Locate platelets.
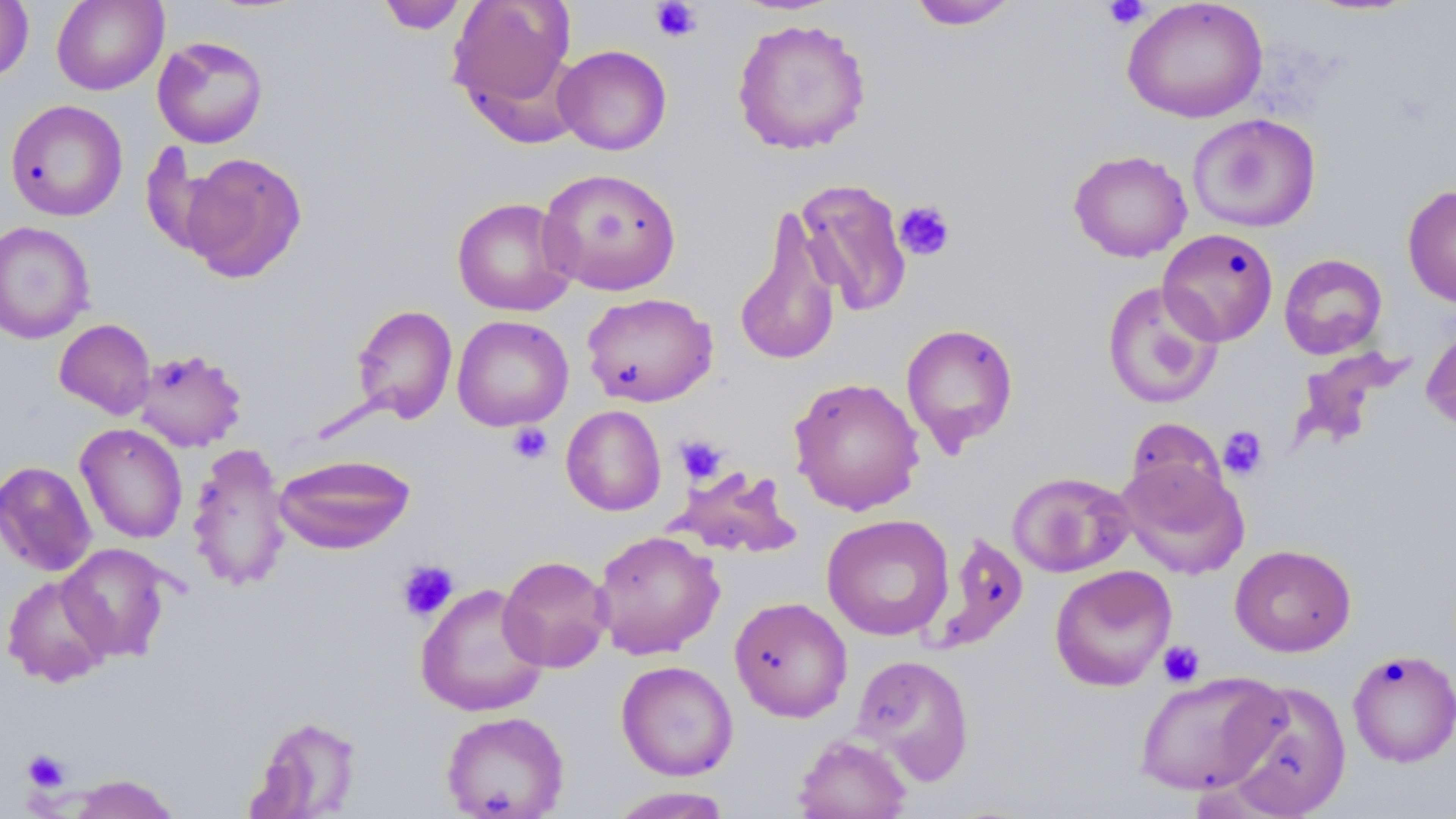

Approximate bounding boxes as (x1, y1, x2, y2) in pixels.
Platelets: (1101, 0, 1151, 31), (649, 1, 703, 43), (893, 200, 956, 260), (507, 422, 552, 465), (1218, 425, 1268, 480), (675, 435, 727, 484), (397, 560, 459, 622), (1157, 640, 1205, 687), (21, 749, 71, 793).

Uninfected red blood cell locations: (0, 0, 34, 82), (52, 0, 168, 95), (447, 0, 579, 122), (1122, 0, 1268, 123), (375, 1, 469, 34), (906, 1, 1020, 31), (731, 17, 873, 156), (152, 35, 269, 149), (553, 44, 672, 155), (5, 99, 128, 222), (1187, 113, 1321, 233), (1068, 149, 1192, 262), (179, 152, 307, 283), (538, 167, 683, 297), (794, 178, 912, 316), (1402, 183, 1456, 309), (451, 196, 578, 316), (733, 210, 843, 367), (0, 221, 95, 344), (1157, 228, 1279, 346), (1278, 253, 1388, 359), (1101, 280, 1223, 409), (581, 292, 718, 407), (351, 304, 458, 424), (452, 315, 574, 432), (54, 318, 156, 419), (1421, 319, 1456, 432), (900, 322, 1020, 455), (1290, 347, 1413, 451), (133, 348, 247, 453), (788, 376, 925, 515), (561, 405, 666, 516), (1125, 418, 1228, 511), (75, 423, 188, 544), (187, 442, 291, 593), (273, 453, 415, 555), (1118, 459, 1249, 579), (0, 460, 97, 577), (669, 466, 801, 559), (1007, 471, 1135, 578), (822, 514, 954, 641), (592, 529, 724, 659), (928, 533, 1028, 652), (57, 543, 174, 662), (1230, 544, 1356, 657), (498, 555, 612, 672), (1049, 564, 1177, 691), (2, 574, 114, 687), (415, 582, 549, 717), (729, 596, 853, 722), (1346, 649, 1456, 767), (851, 654, 975, 783), (616, 660, 738, 781), (1133, 672, 1287, 796), (1221, 679, 1351, 818), (440, 711, 570, 819), (245, 714, 363, 817), (793, 733, 912, 819), (63, 774, 182, 818), (607, 787, 733, 818). Slide-level diagnosis: no evidence of blood parasites. Thin blood film. 1000x magnification. Single field of view. Image is 1456×819 pixels. Optical microscopy. May-Grünwald-Giemsa-stained preparation.